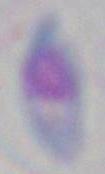
{
  "identification": "Toxoplasma gondii",
  "modality": "micrograph",
  "magnification": "1000x"
}